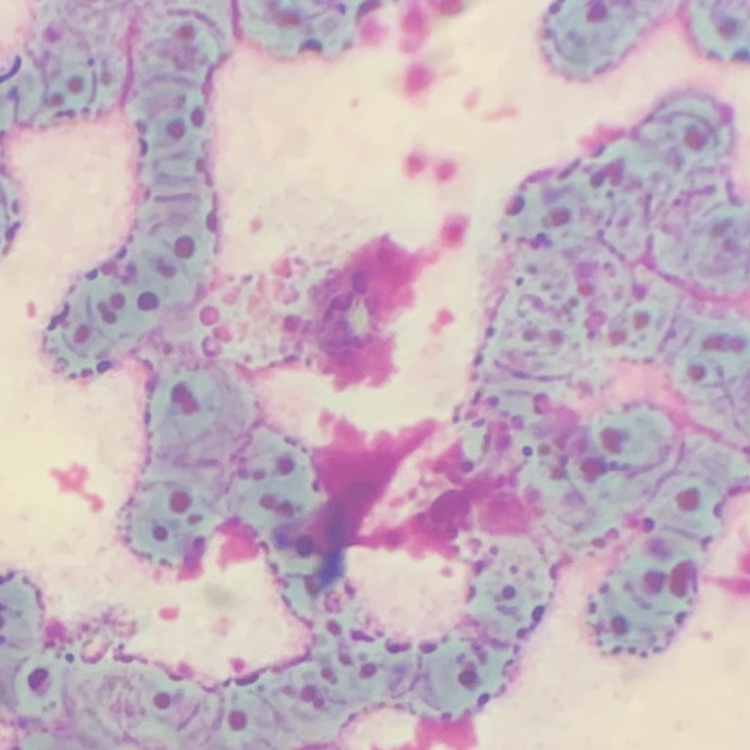

erythrocyte morphology = rouleaux formation
stain = Field's or Giemsa
preparation = thin blood film
image type = square crop of a larger photomicrograph